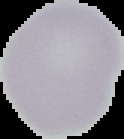
preparation: thin blood smear
image_size: 124×139 pixels
result: no malaria parasites detected
image_type: cell region segmented out of the field of view; surrounding area masked to black